Comment on the morphology of the erythrocytes.
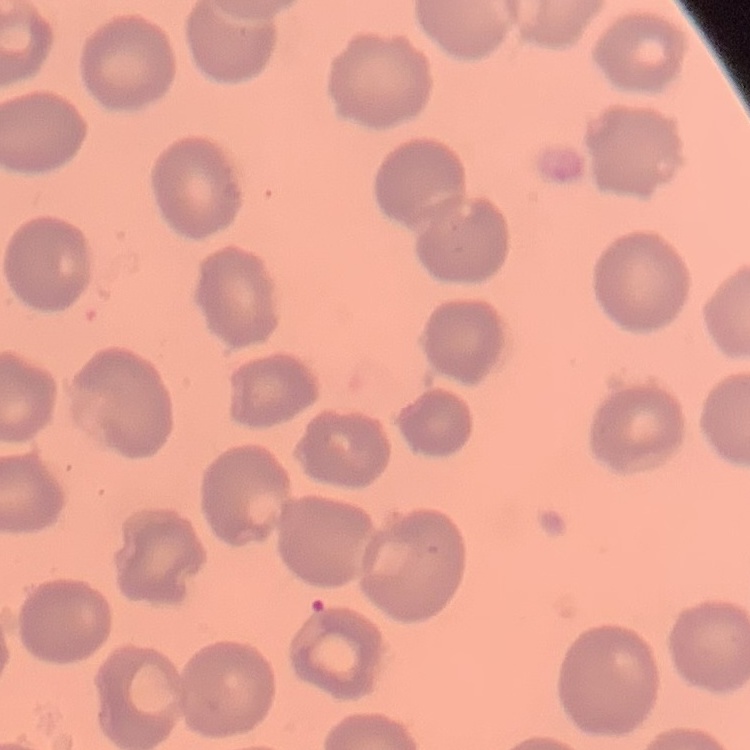
No rouleaux formation.

stain = Field's or Giemsa
preparation = thin peripheral smear
image type = square crop of a larger photomicrograph